State which parasite is depicted.
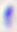
Toxoplasma gondii.

modality = micrograph
magnification = 400x